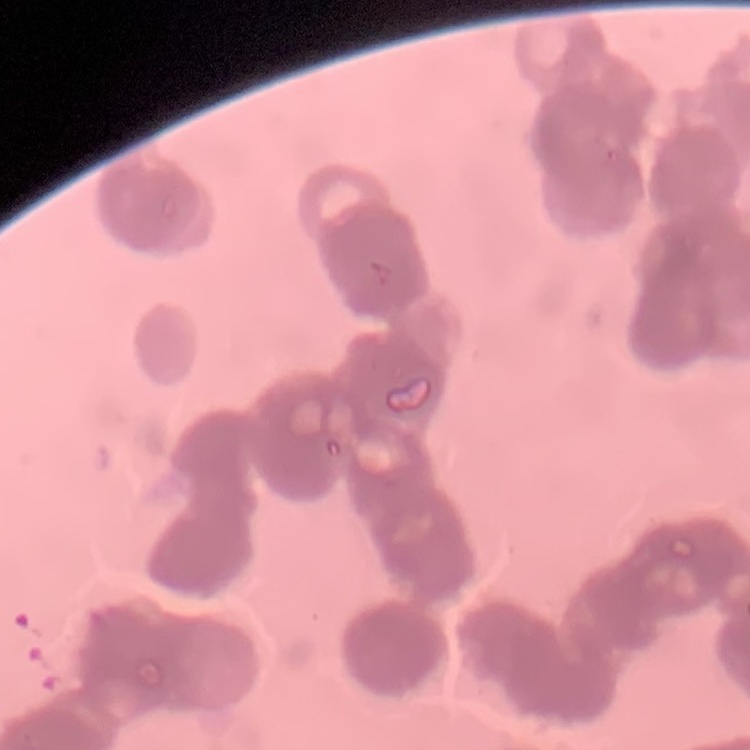
The red blood cells show rouleaux formation. Field's or Giemsa stain. Thin blood smear. Square crop of a larger photomicrograph.